Classify this cell by malaria status.
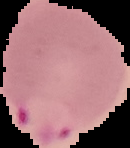

It is parasitized.

image size = 130×148 pixels
preparation = thin blood smear
image type = segmented cell region on a black background